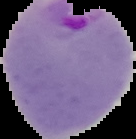
Summary:
  - Image size: 136×139 pixels
  - Result: Plasmodium parasites detected
  - Preparation: thin blood film
  - Image type: cell region segmented out of the field of view; surrounding area masked to black